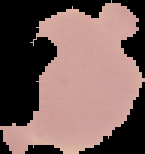

preparation: thin blood film
image_size: 145×154 pixels
image_type: cell region segmented out of the field of view; surrounding area masked to black
malaria_status: uninfected